Outline each Plasmodium ovale-infected red blood cell.
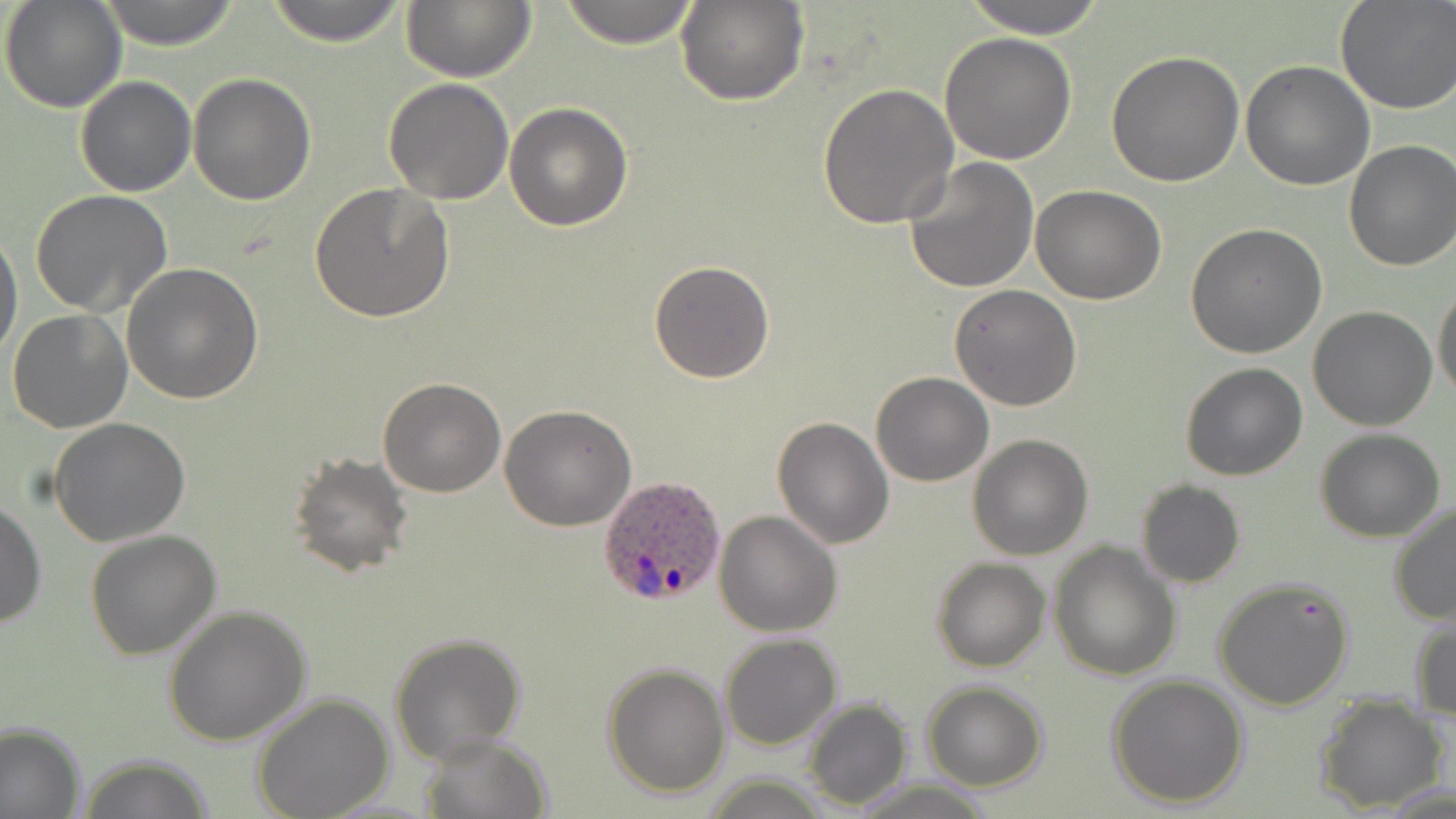
Approximate bounding boxes as named x1/y1/x2/y2 corners in pixels.
Plasmodium ovale-infected red blood cells: (x1=596, y1=475, x2=728, y2=608).

Summary:
  - Uninfected red blood cell locations: (x1=2, y1=0, x2=128, y2=114), (x1=99, y1=0, x2=242, y2=49), (x1=263, y1=0, x2=411, y2=46), (x1=401, y1=0, x2=534, y2=83), (x1=556, y1=0, x2=702, y2=48), (x1=961, y1=0, x2=1113, y2=39), (x1=678, y1=1, x2=806, y2=106), (x1=1334, y1=1, x2=1456, y2=115), (x1=939, y1=31, x2=1077, y2=164), (x1=1104, y1=51, x2=1245, y2=187), (x1=1240, y1=61, x2=1375, y2=191), (x1=187, y1=72, x2=316, y2=207), (x1=75, y1=75, x2=196, y2=196), (x1=383, y1=79, x2=514, y2=204), (x1=817, y1=83, x2=958, y2=228), (x1=505, y1=101, x2=634, y2=231), (x1=1342, y1=140, x2=1456, y2=270), (x1=902, y1=155, x2=1039, y2=294), (x1=312, y1=183, x2=454, y2=322), (x1=1031, y1=184, x2=1166, y2=304), (x1=31, y1=191, x2=174, y2=320), (x1=1185, y1=222, x2=1327, y2=360), (x1=0, y1=227, x2=23, y2=366), (x1=649, y1=260, x2=776, y2=384), (x1=120, y1=261, x2=265, y2=404), (x1=1432, y1=283, x2=1456, y2=402), (x1=948, y1=284, x2=1082, y2=411), (x1=1308, y1=306, x2=1437, y2=431), (x1=6, y1=309, x2=132, y2=433), (x1=1180, y1=363, x2=1308, y2=481), (x1=869, y1=372, x2=994, y2=487), (x1=378, y1=378, x2=506, y2=497), (x1=500, y1=405, x2=636, y2=531), (x1=771, y1=417, x2=893, y2=550), (x1=48, y1=418, x2=191, y2=545), (x1=1315, y1=427, x2=1445, y2=542), (x1=967, y1=433, x2=1093, y2=558), (x1=289, y1=453, x2=414, y2=578), (x1=1135, y1=481, x2=1245, y2=588), (x1=1, y1=498, x2=45, y2=632), (x1=1388, y1=500, x2=1456, y2=627), (x1=713, y1=510, x2=842, y2=637), (x1=84, y1=530, x2=224, y2=660), (x1=1049, y1=542, x2=1181, y2=683), (x1=932, y1=558, x2=1050, y2=672), (x1=1212, y1=576, x2=1356, y2=711), (x1=164, y1=604, x2=311, y2=745), (x1=1410, y1=619, x2=1456, y2=724), (x1=387, y1=633, x2=527, y2=764), (x1=720, y1=634, x2=842, y2=751), (x1=601, y1=662, x2=730, y2=798), (x1=1107, y1=674, x2=1250, y2=809), (x1=921, y1=680, x2=1049, y2=791), (x1=249, y1=692, x2=394, y2=819), (x1=1313, y1=693, x2=1449, y2=814), (x1=804, y1=698, x2=913, y2=810), (x1=0, y1=722, x2=85, y2=819), (x1=423, y1=736, x2=551, y2=818), (x1=73, y1=754, x2=217, y2=818), (x1=698, y1=773, x2=834, y2=818)
  - Slide-level diagnosis: Plasmodium ovale
  - Image size: 1456×819 pixels
  - Stain: May-Grünwald-Giemsa
  - Field of view: one of a larger specimen
  - Magnification: 1000x
  - Preparation: thin blood film
  - Modality: optical microscopy